Classify this cell by malaria status.
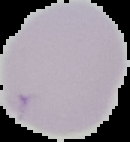

It is uninfected.

Summary:
  - Preparation: thin blood film
  - Image size: 130×142 pixels
  - Image type: segmented cell region on a black background